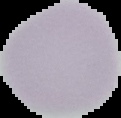
image type = segmented cell region on a black background
preparation = thin blood film
result = negative for Plasmodium parasites
image size = 121×118 pixels